Locate every blood parasite and identify its species.
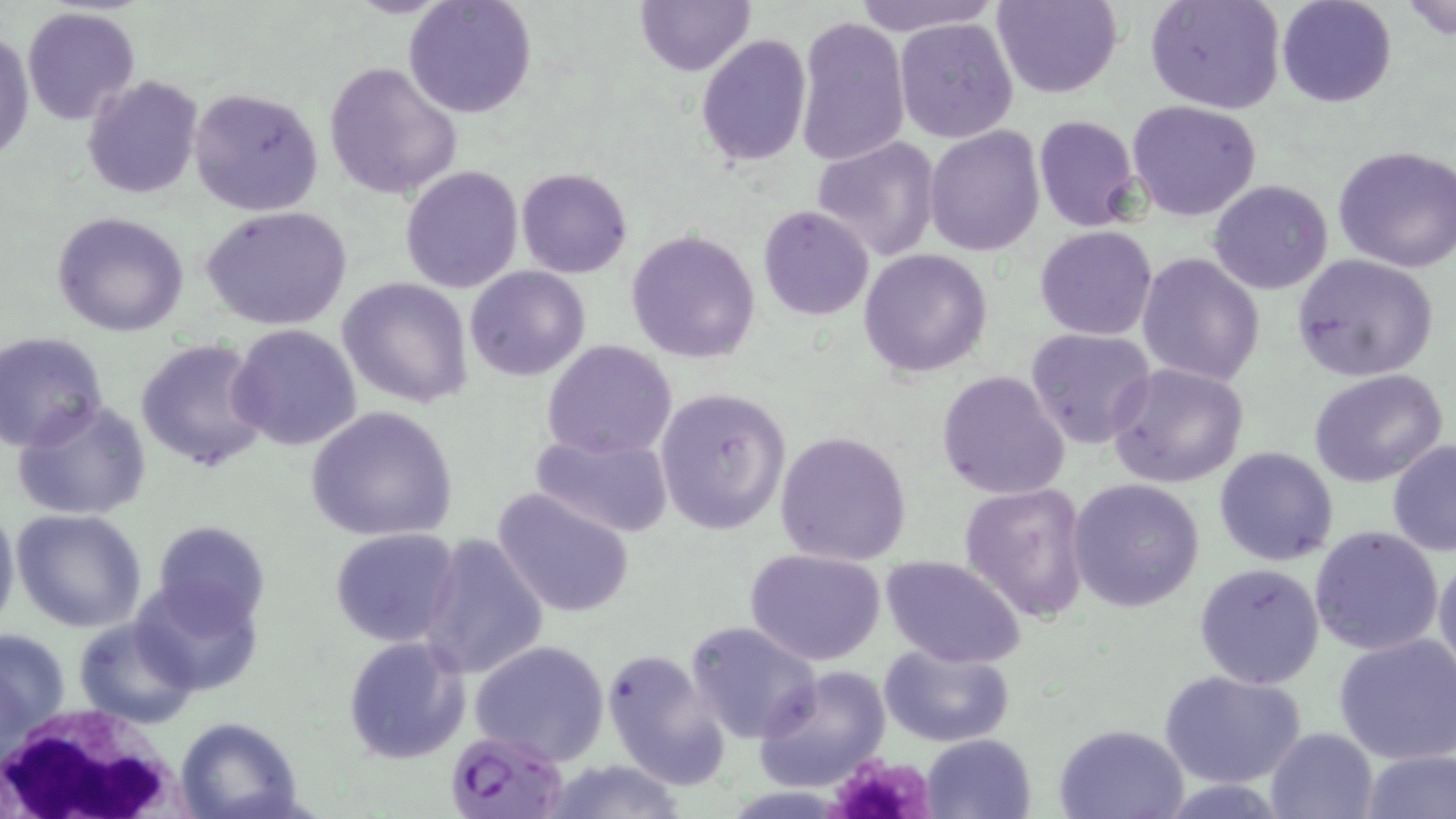

Approximate bounding boxes as [x1, y1, x2, y2] in pixels.
Plasmodium falciparum-infected red blood cells: [450, 729, 568, 815].
No Plasmodium ovale, Plasmodium malariae, Plasmodium vivax, Babesia divergens, or Trypanosoma brucei observed.

slide-level diagnosis = Plasmodium falciparum
preparation = thin blood film
magnification = 1000x
field of view = one of a larger specimen
image size = 1456×819 pixels
stain = May-Grünwald-Giemsa
modality = optical microscopy
platelet locations = approximate bounding boxes as [x1, y1, x2, y2] in pixels: [826, 752, 934, 819]
white blood cell locations = approximate bounding boxes as [x1, y1, x2, y2] in pixels: [0, 699, 191, 818]
uninfected red blood cell locations = approximate bounding boxes as [x1, y1, x2, y2] in pixels: [404, 0, 537, 118], [634, 0, 755, 75], [847, 0, 1000, 36], [993, 0, 1121, 99], [1143, 0, 1286, 115], [1402, 0, 1456, 38], [1275, 1, 1396, 109], [22, 7, 141, 126], [795, 16, 910, 166], [893, 16, 1020, 142], [1, 25, 34, 166], [695, 34, 812, 165], [321, 62, 461, 199], [81, 76, 203, 201], [188, 86, 324, 216], [1127, 100, 1262, 221], [1032, 115, 1142, 232], [923, 127, 1044, 255], [812, 136, 940, 263], [1333, 143, 1456, 272], [399, 165, 523, 293], [516, 168, 632, 278], [1208, 179, 1332, 295], [200, 205, 352, 330], [758, 206, 874, 319], [52, 211, 189, 337], [1034, 225, 1158, 341], [625, 228, 761, 364], [858, 247, 992, 378], [1136, 253, 1266, 386], [1292, 254, 1440, 382], [465, 266, 589, 380], [338, 277, 474, 409], [227, 323, 364, 451], [1025, 327, 1158, 449], [0, 331, 107, 452], [135, 338, 270, 472], [541, 340, 678, 460], [1107, 362, 1249, 488], [936, 369, 1072, 499], [1308, 369, 1449, 489], [653, 387, 791, 535], [11, 400, 152, 520], [305, 405, 458, 542], [530, 429, 673, 536], [774, 429, 914, 566], [1387, 438, 1456, 557], [1214, 446, 1338, 566], [1067, 478, 1206, 611], [959, 482, 1091, 624], [493, 487, 634, 617], [0, 498, 20, 639], [11, 508, 148, 631], [147, 520, 268, 634], [1307, 524, 1443, 655], [329, 526, 462, 647], [418, 532, 549, 680], [745, 547, 886, 665], [1433, 550, 1456, 684], [878, 554, 1027, 670], [1194, 563, 1325, 689], [131, 579, 264, 698], [74, 615, 198, 727], [684, 621, 824, 746], [1, 626, 71, 748], [342, 633, 473, 763], [1332, 633, 1456, 764], [468, 640, 611, 767], [879, 642, 1015, 748], [602, 645, 732, 790], [752, 664, 892, 791], [1159, 670, 1308, 788], [174, 716, 305, 819], [1053, 722, 1189, 817], [1265, 726, 1381, 818], [921, 734, 1036, 819], [1357, 747, 1454, 819], [537, 758, 690, 818]